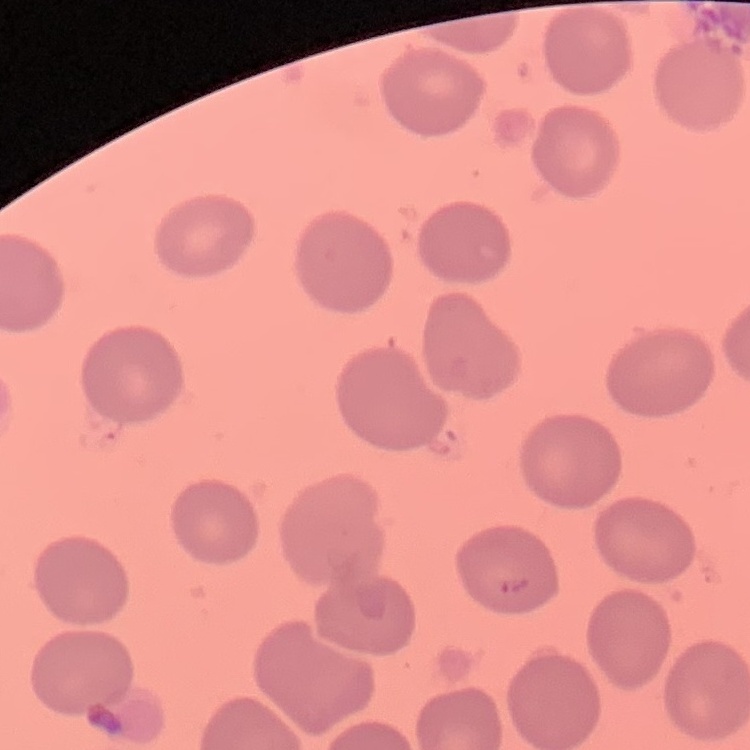
Summary:
  - Red blood cell morphology: no rouleaux formation
  - Preparation: thin blood film
  - Stain: Field's or Giemsa
  - Image type: one tile cut from a larger photomicrograph